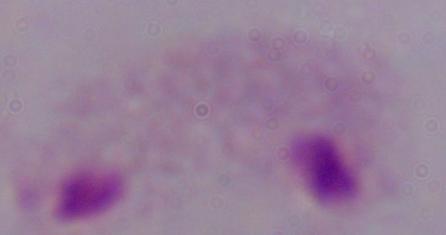
magnification = 1000x
identification = trichomonad
modality = photomicrograph